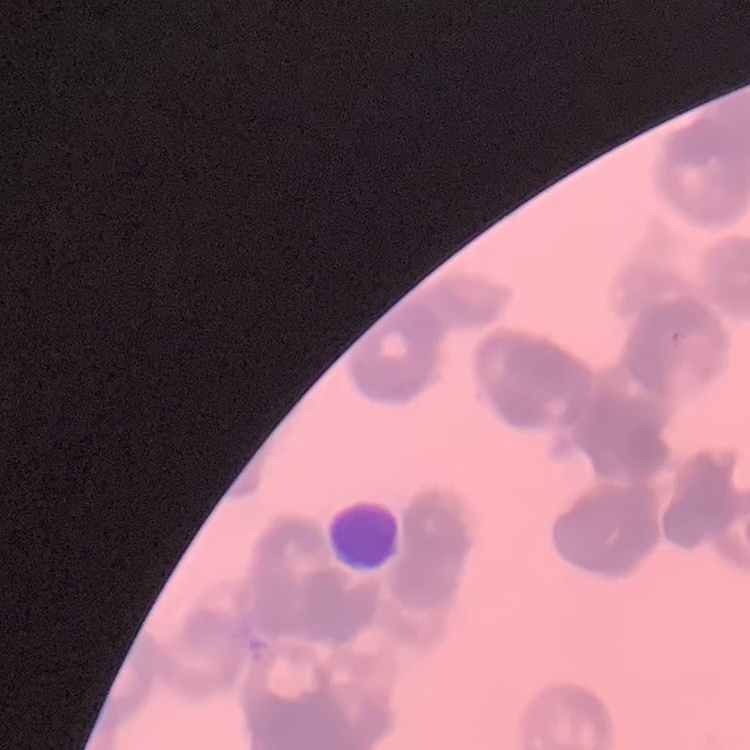

{
  "red_blood_cell_morphology": "rouleaux formation",
  "preparation": "thin blood film",
  "stain": "Field's or Giemsa",
  "image_type": "square crop of a larger photomicrograph"
}